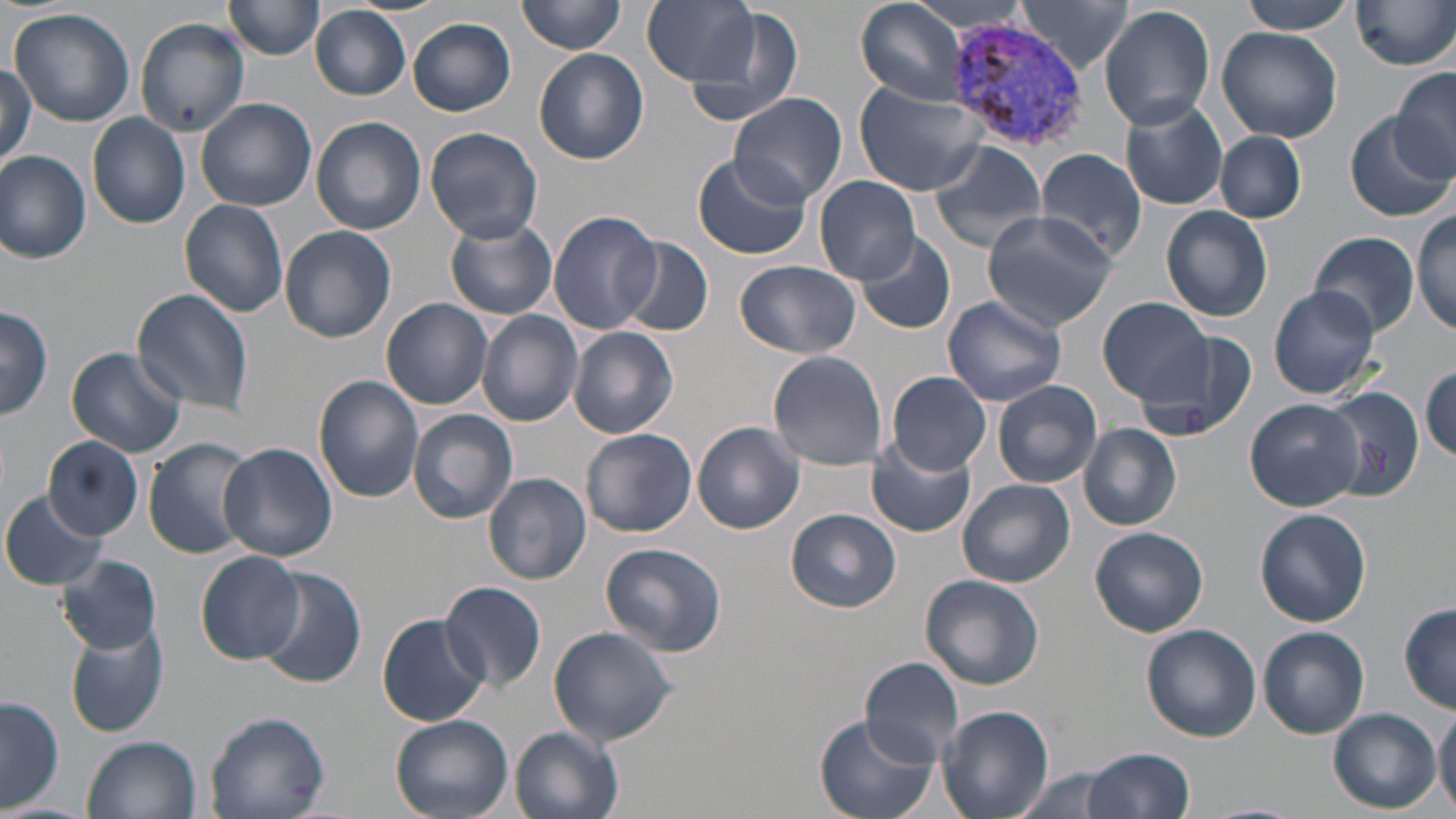

slide-level diagnosis = Plasmodium vivax
preparation = thin blood smear
image size = 1456×819 pixels
modality = optical microscopy
uninfected red blood cell locations = approximate bounding boxes as [x1, y1, x2, y2] in pixels: [223, 0, 325, 59], [517, 0, 628, 54], [856, 0, 973, 106], [1018, 0, 1132, 74], [1237, 0, 1357, 35], [641, 1, 762, 88], [904, 1, 1034, 35], [1352, 1, 1456, 71], [1098, 5, 1216, 130], [312, 6, 411, 101], [678, 7, 806, 129], [9, 8, 136, 128], [133, 16, 251, 136], [408, 18, 516, 116], [1217, 26, 1343, 142], [534, 49, 649, 165], [0, 64, 35, 171], [1390, 66, 1456, 181], [857, 83, 986, 195], [729, 92, 847, 206], [196, 98, 317, 211], [1118, 99, 1229, 210], [86, 112, 191, 228], [1343, 113, 1451, 222], [311, 117, 427, 235], [423, 126, 543, 243], [1216, 132, 1305, 223], [926, 139, 1049, 252], [0, 149, 91, 264], [1034, 149, 1149, 266], [692, 152, 811, 261], [815, 175, 921, 286], [179, 199, 289, 319], [1162, 207, 1273, 323], [981, 209, 1116, 331], [1413, 209, 1455, 335], [547, 210, 663, 336], [444, 217, 557, 319], [279, 225, 396, 344], [855, 230, 956, 334], [1310, 231, 1419, 337], [617, 236, 713, 337], [734, 259, 862, 358], [1267, 285, 1383, 400], [131, 288, 258, 415], [943, 294, 1066, 405], [381, 296, 494, 410], [1100, 297, 1215, 407], [0, 306, 53, 421], [478, 311, 584, 427], [1138, 324, 1255, 446], [567, 327, 680, 438], [67, 347, 187, 458], [768, 350, 888, 469], [1419, 365, 1455, 464], [888, 371, 990, 475], [313, 375, 425, 503], [993, 380, 1102, 488], [1322, 386, 1425, 503], [1245, 399, 1363, 511], [410, 409, 518, 526], [693, 421, 806, 534], [1079, 423, 1182, 530], [582, 429, 697, 537], [44, 436, 143, 539], [142, 438, 259, 558], [865, 438, 976, 537], [218, 442, 338, 563], [484, 472, 591, 584], [958, 478, 1076, 587], [1, 490, 108, 590], [785, 508, 902, 613], [1255, 508, 1371, 628], [1090, 526, 1209, 637], [599, 542, 727, 658], [196, 551, 303, 663], [56, 553, 162, 655], [257, 566, 367, 690], [920, 574, 1045, 690], [441, 581, 547, 691], [1398, 603, 1456, 714], [378, 612, 490, 728], [1141, 624, 1262, 741], [64, 625, 168, 737], [548, 626, 679, 746], [1257, 627, 1370, 738], [862, 657, 967, 767], [1, 696, 63, 812], [1434, 701, 1456, 815], [936, 705, 1053, 819], [1327, 707, 1441, 812], [206, 712, 329, 819], [813, 712, 937, 819], [388, 713, 513, 819], [511, 726, 625, 819], [84, 734, 202, 819], [1082, 746, 1194, 818], [1004, 767, 1129, 819], [1197, 801, 1303, 819]
Plasmodium vivax-infected red blood cell locations = approximate bounding boxes as [x1, y1, x2, y2] in pixels: [943, 18, 1092, 155]
magnification = 1000x
stain = May-Grünwald-Giemsa
field of view = one of a larger specimen